Name the parasite shown.
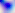
This is Toxoplasma gondii.

Micrograph. 400x magnification.